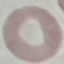
Malaria status: uninfected. Thin blood film. Automatically extracted cell patch, resized to 64 × 64 pixels. Photographed with a smartphone camera at the microscope eyepiece. Giemsa stain.